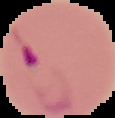
Summary:
  - Malaria status: parasitized
  - Image type: segmented cell region with the area outside set to black
  - Image size: 115×118 pixels
  - Preparation: thin blood film